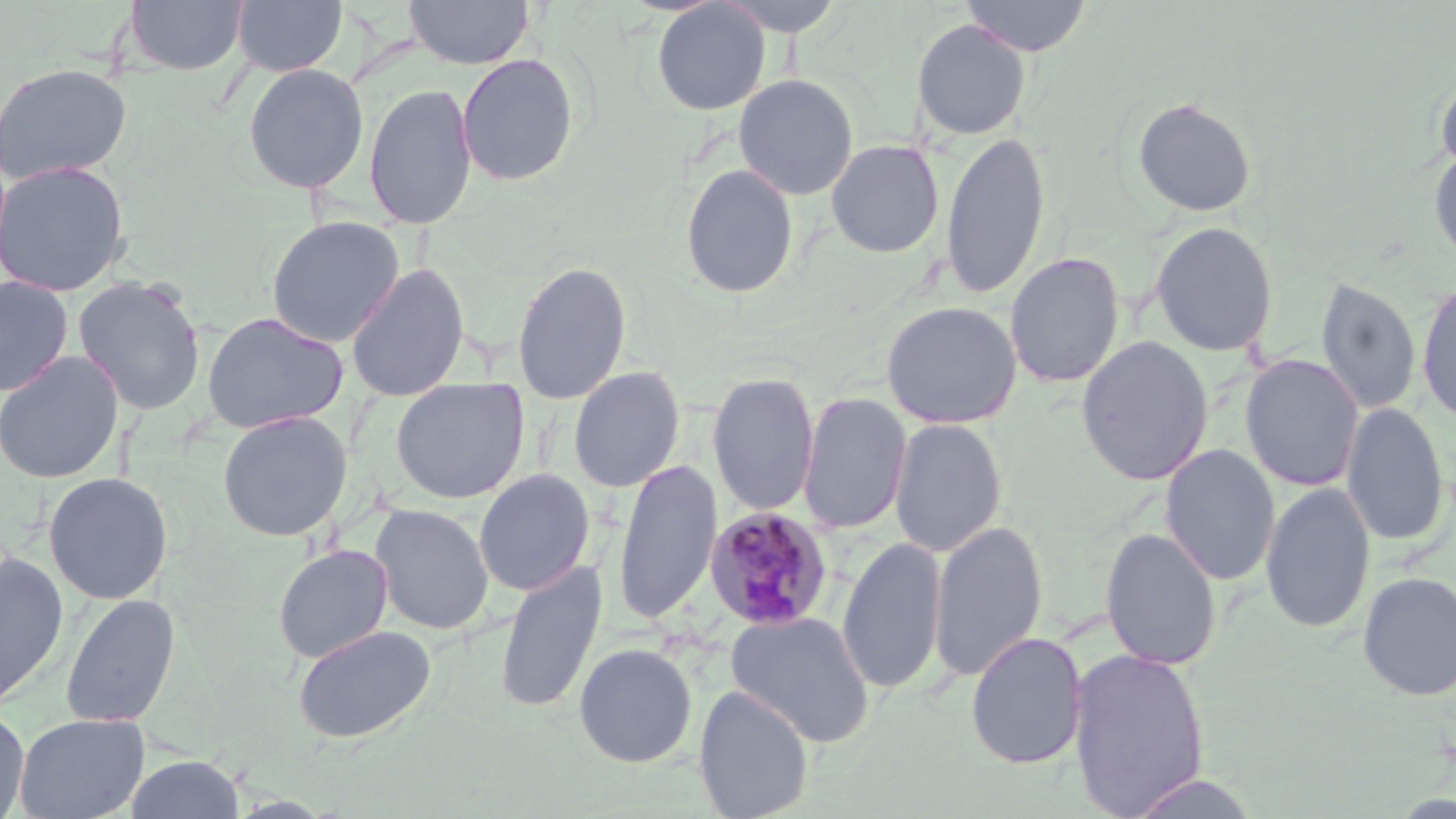
slide_level_diagnosis: Plasmodium malariae
image_size: 1456×819 pixels
plasmodium_malariae_infected_red_blood_cell_locations: 'approximate bounding boxes as (x1,y1)-(x2,y2) corner pairs in pixels: (704,507)-(834,631)'
magnification: 1000x
field_of_view: one of a larger specimen
stain: May-Grünwald-Giemsa
modality: light microscopy
preparation: thin blood smear
uninfected_red_blood_cell_locations: 'approximate bounding boxes as (x1,y1)-(x2,y2) corner pairs in pixels: (124,0)-(249,76), (231,0)-(348,77), (404,0)-(534,69), (713,0)-(849,36), (960,0)-(1093,56), (651,1)-(770,116), (912,18)-(1031,140), (456,53)-(579,186), (0,62)-(133,186), (243,63)-(369,194), (1434,72)-(1456,178), (733,74)-(858,201), (364,82)-(477,230), (1132,96)-(1257,218), (941,129)-(1051,300), (826,139)-(944,258), (1428,148)-(1456,267), (0,160)-(130,297), (680,163)-(799,299), (265,215)-(405,347), (1149,221)-(1279,357), (1005,251)-(1124,389), (512,260)-(632,405), (346,262)-(470,402), (0,275)-(73,396), (73,276)-(207,415), (1315,276)-(1422,416), (1416,280)-(1456,424), (881,301)-(1022,429), (201,311)-(348,434), (1076,336)-(1214,486), (0,351)-(123,484), (1241,355)-(1364,492), (568,365)-(686,493), (707,371)-(819,517), (390,377)-(529,504), (798,391)-(911,534), (1341,402)-(1450,547), (217,410)-(352,541), (889,418)-(1007,557), (1160,445)-(1280,586), (613,458)-(723,626), (474,468)-(594,596), (43,472)-(173,605), (1260,481)-(1376,634), (370,503)-(494,636), (929,520)-(1048,683), (1100,526)-(1222,671), (837,537)-(947,696), (273,544)-(393,663), (0,550)-(69,709), (495,559)-(608,715), (1357,571)-(1456,702), (60,593)-(180,728), (725,611)-(875,746), (293,624)-(436,743), (966,631)-(1087,770), (573,642)-(697,767), (1068,646)-(1210,817), (693,685)-(815,819), (0,707)-(30,818), (14,713)-(149,819), (125,754)-(245,818), (1124,772)-(1261,817)'